Assess this cell for malaria.
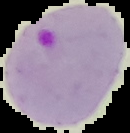
Parasitized.

preparation = thin blood film
image size = 130×133 pixels
image type = cell region segmented out of the field of view; surrounding area masked to black